Comment on the morphology of the erythrocytes.
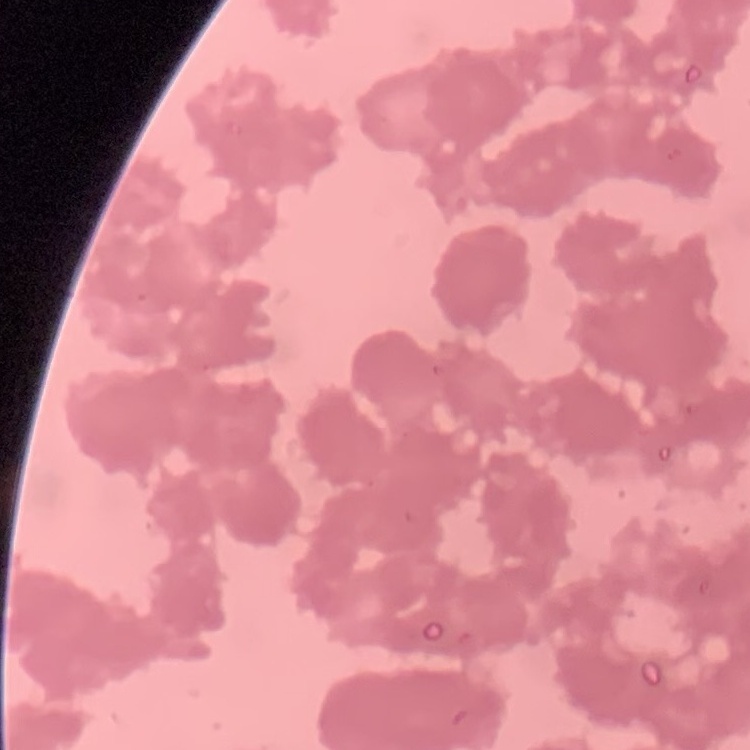
They show rouleaux formation.

Thin blood smear. Stained with either Field's or Giemsa. One tile cut from a larger photomicrograph.